Name the cell type shown.
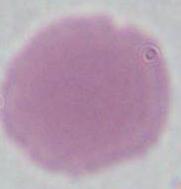
An erythrocyte.

Summary:
  - Modality: micrograph
  - Magnification: 1000x